Report the malaria status.
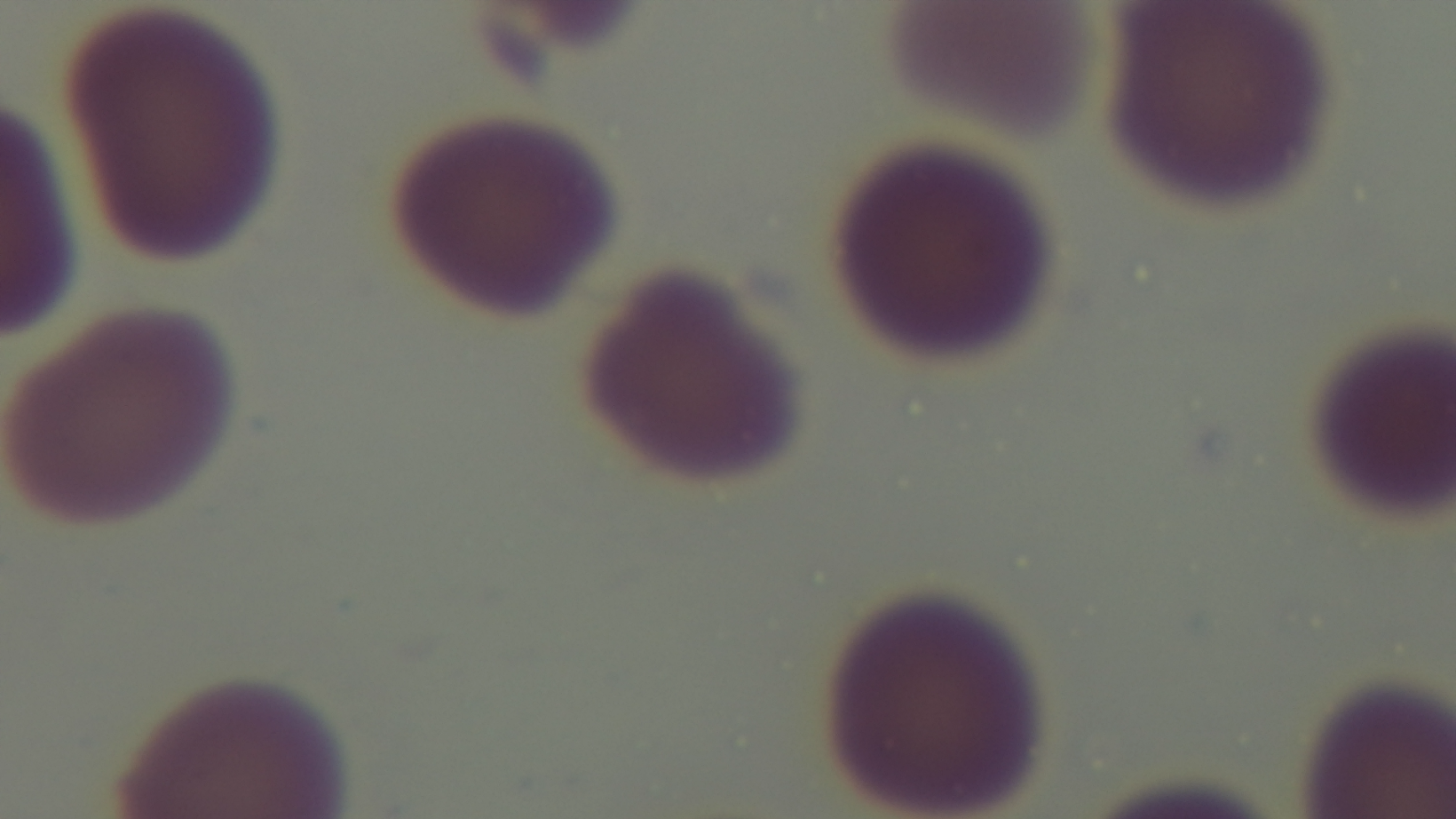

Uninfected.

Summary:
  - Objective: 100x oil immersion
  - Modality: light microscopy
  - Field of view: single
  - Stain: Giemsa
  - Preparation: thin
  - Capture: mounted 4K digital camera